Assess this cell for malaria.
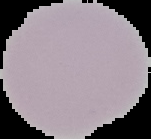

It is uninfected.

Summary:
  - Image size: 151×139 pixels
  - Image type: segmented cell region on a black background
  - Preparation: thin blood film